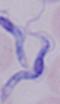
Summary:
  - Magnification: 1000x
  - Identification: trypanosome
  - Modality: photomicrograph